Name the blood parasite species.
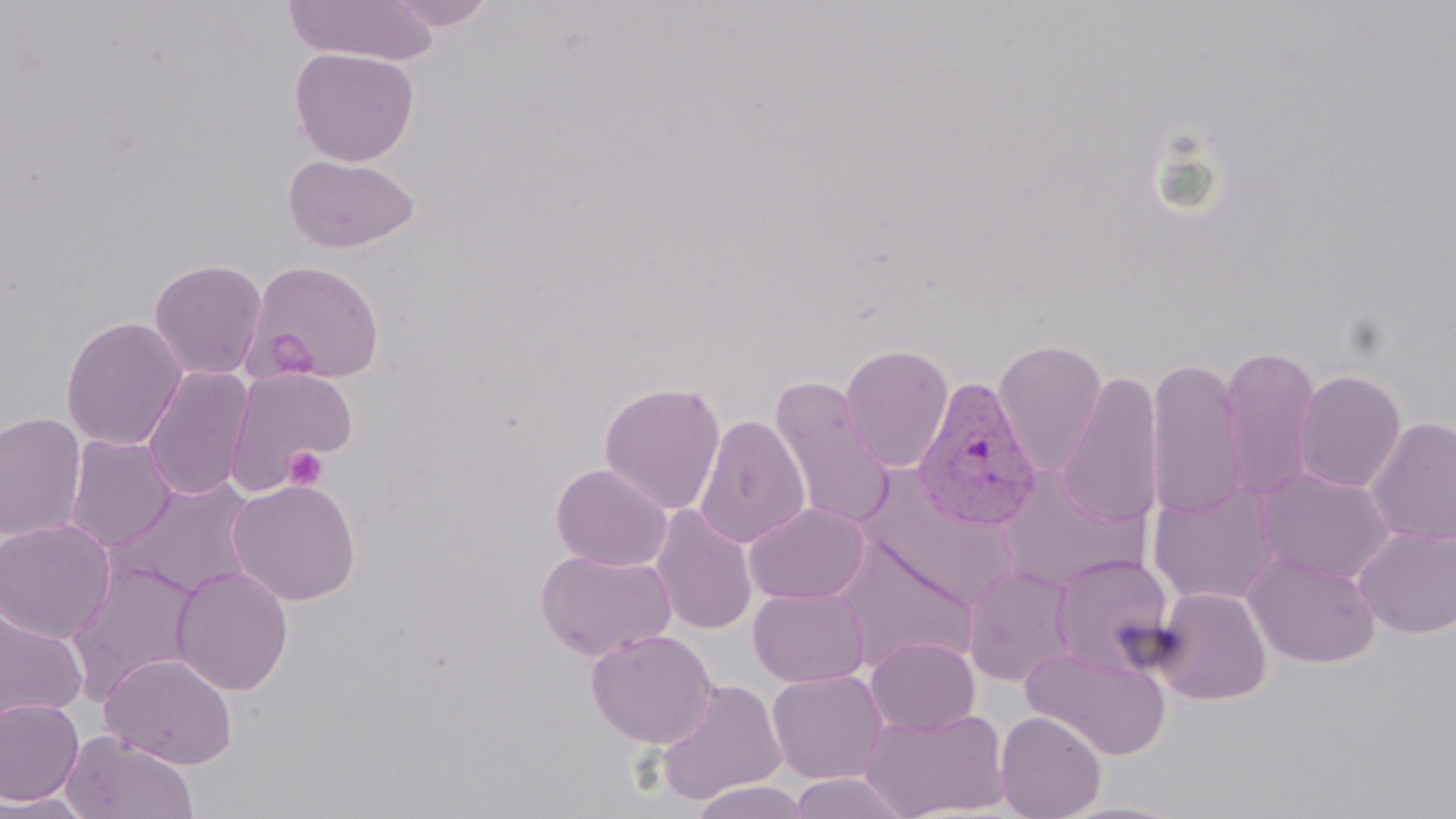
Plasmodium vivax.

Approximate bounding boxes as [x1, y1, x2, y2] in pixels. Plasmodium vivax-infected red blood cell locations: [910, 376, 1044, 533]. Uninfected red blood cell locations: [282, 0, 440, 65], [386, 0, 496, 31], [289, 46, 420, 166], [283, 154, 420, 253], [148, 258, 268, 380], [248, 260, 385, 383], [61, 316, 188, 451], [992, 339, 1108, 476], [839, 343, 954, 472], [1217, 343, 1323, 502], [1145, 355, 1247, 524], [142, 366, 253, 502], [224, 367, 357, 492], [1293, 369, 1407, 493], [1055, 370, 1165, 531], [768, 377, 897, 531], [598, 380, 726, 515], [0, 411, 86, 542], [694, 415, 810, 548], [1365, 416, 1456, 546], [64, 435, 178, 552], [550, 463, 672, 571], [1256, 467, 1396, 584], [995, 474, 1144, 593], [858, 476, 1019, 607], [109, 477, 258, 599], [227, 479, 362, 605], [1148, 482, 1283, 607], [744, 502, 870, 605], [651, 505, 757, 635], [0, 519, 117, 644], [1353, 524, 1456, 638], [831, 538, 979, 674], [535, 548, 676, 662], [1049, 552, 1176, 676], [1243, 552, 1380, 668], [66, 560, 204, 703], [961, 564, 1078, 687], [171, 565, 294, 696], [747, 586, 870, 688], [1152, 586, 1271, 706], [1, 603, 89, 723], [585, 629, 718, 748], [865, 637, 980, 736], [1021, 643, 1171, 760], [100, 653, 238, 769], [767, 669, 889, 785], [654, 680, 787, 806], [0, 697, 85, 807], [860, 705, 1010, 818], [995, 710, 1107, 819], [62, 731, 198, 819], [786, 772, 913, 818], [688, 781, 814, 818], [0, 792, 95, 818]. Platelet locations: [263, 328, 318, 380], [284, 446, 329, 491]. Image is 1456×819 pixels. Single field of view. Light microscopy. Captured at 1000x magnification. Thin blood film. May-Grünwald-Giemsa-stained preparation.